Identify the blood parasite species.
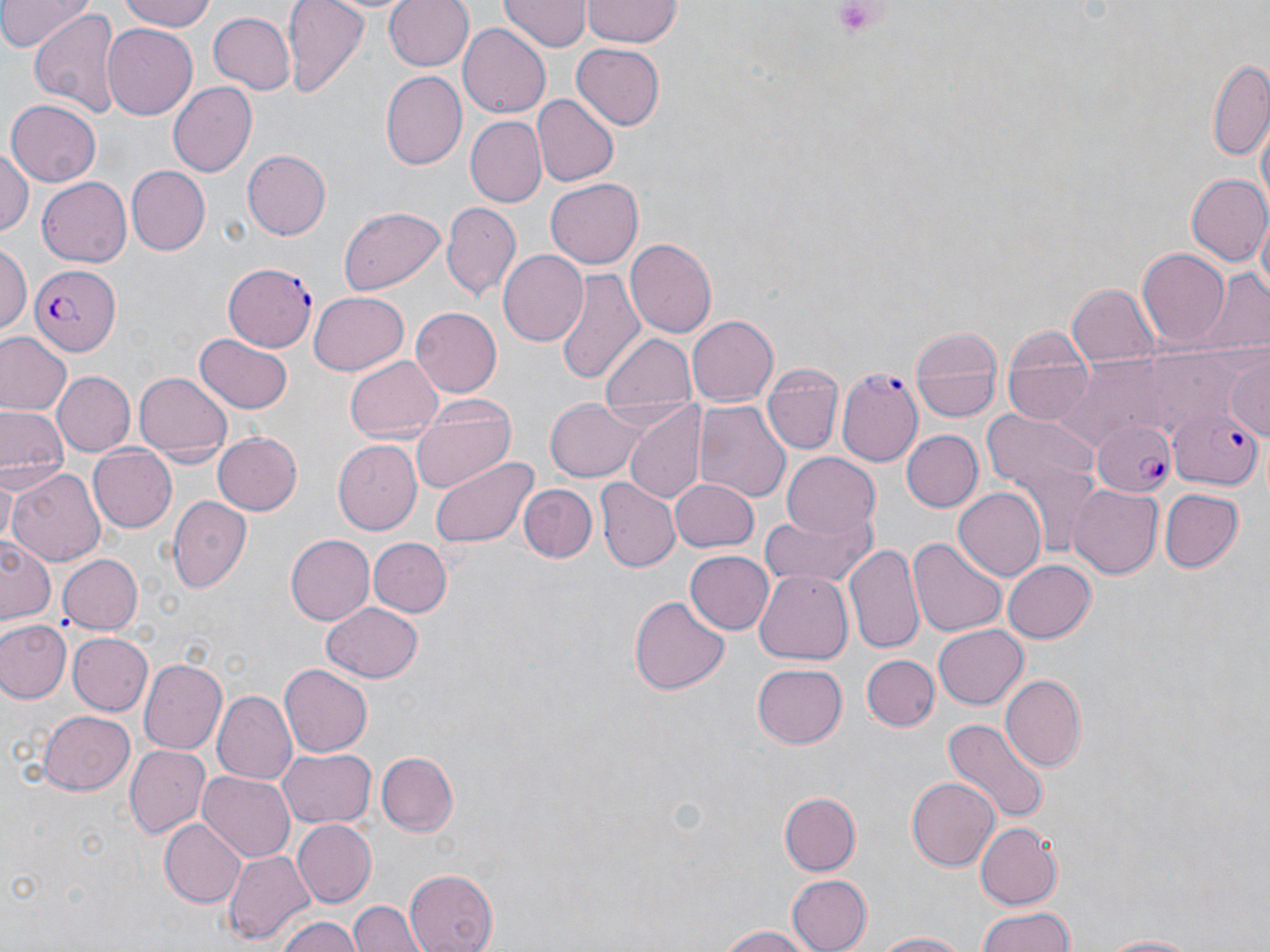
Plasmodium falciparum.

preparation = thin blood film
field of view = one of a larger specimen
uninfected red blood cell locations = approximate bounding boxes as (x1, y1, x2, y2) in pixels: (0, 0, 89, 50), (120, 0, 220, 31), (282, 0, 369, 94), (383, 0, 472, 73), (499, 1, 588, 53), (581, 1, 683, 46), (28, 6, 121, 118), (207, 11, 296, 94), (102, 24, 198, 120), (458, 25, 551, 116), (571, 41, 666, 130), (1206, 61, 1269, 163), (380, 72, 464, 171), (167, 81, 257, 177), (533, 95, 619, 186), (6, 99, 100, 187), (466, 117, 546, 205), (0, 149, 34, 239), (242, 149, 330, 240), (126, 166, 208, 255), (1185, 173, 1270, 267), (37, 175, 132, 268), (547, 176, 643, 267), (442, 203, 521, 298), (339, 206, 446, 295), (1254, 214, 1269, 306), (627, 239, 717, 337), (0, 245, 29, 337), (1136, 247, 1231, 351), (499, 250, 589, 346), (554, 268, 646, 387), (1193, 269, 1270, 356), (1066, 283, 1159, 370), (309, 290, 409, 374), (411, 309, 501, 397), (687, 315, 778, 406), (1000, 323, 1093, 428), (907, 326, 1003, 425), (599, 331, 699, 413), (0, 332, 71, 415), (197, 332, 292, 411), (1226, 354, 1270, 437), (344, 356, 444, 445), (762, 367, 842, 456), (52, 371, 134, 457), (135, 372, 231, 463), (545, 397, 646, 481), (410, 399, 519, 491), (694, 404, 789, 506), (0, 405, 64, 482), (624, 407, 706, 503), (980, 410, 1101, 498), (901, 429, 983, 513), (213, 431, 302, 516), (332, 441, 422, 536), (87, 443, 178, 533), (428, 453, 538, 550), (781, 454, 882, 542), (8, 467, 106, 569), (2, 474, 19, 546), (668, 479, 758, 552), (597, 480, 678, 572), (520, 483, 596, 562), (1068, 484, 1163, 580), (954, 487, 1048, 581), (1159, 489, 1242, 574), (169, 496, 251, 594), (759, 510, 877, 591), (1, 535, 58, 626), (284, 535, 374, 625), (908, 536, 1009, 638), (367, 537, 451, 618), (843, 544, 924, 658), (683, 549, 774, 636), (59, 554, 142, 635), (1001, 558, 1096, 644), (753, 566, 852, 662), (630, 594, 727, 697), (322, 602, 423, 681), (0, 620, 71, 704), (932, 623, 1027, 709), (65, 632, 152, 717), (862, 654, 939, 731), (137, 658, 228, 757), (278, 664, 372, 757), (752, 664, 848, 749), (999, 676, 1086, 774), (214, 689, 299, 783), (38, 711, 134, 794), (943, 717, 1047, 829), (123, 744, 210, 838), (275, 747, 374, 828), (377, 751, 458, 836), (198, 771, 295, 861), (905, 775, 1001, 870), (778, 791, 860, 875), (159, 818, 246, 907), (293, 819, 375, 906), (976, 821, 1063, 909), (225, 849, 313, 944), (403, 870, 496, 952), (786, 875, 871, 951), (349, 899, 423, 952), (972, 907, 1078, 951), (278, 914, 361, 952), (710, 922, 820, 952), (873, 930, 977, 951), (1089, 933, 1211, 951)
platelet locations = approximate bounding boxes as (x1, y1, x2, y2) in pixels: (831, 0, 884, 43)
Plasmodium falciparum-infected red blood cell locations = approximate bounding boxes as (x1, y1, x2, y2) in pixels: (224, 262, 319, 350), (28, 265, 118, 355), (838, 369, 923, 466), (1167, 403, 1264, 489), (1091, 414, 1179, 499)
stain = May-Grünwald-Giemsa
modality = optical microscopy
magnification = 1000x
image size = 1270×952 pixels